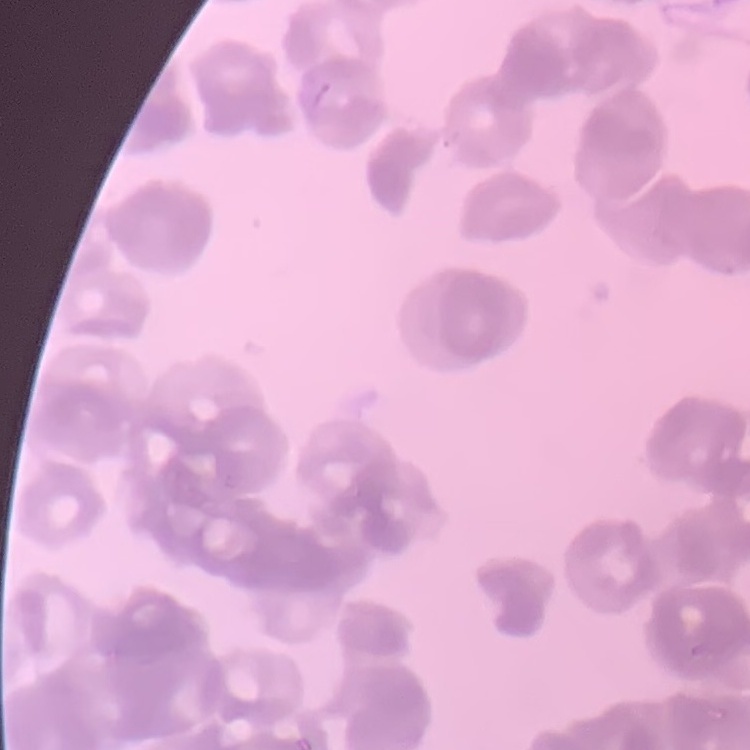
{
  "erythrocyte_morphology": "rouleaux formation",
  "preparation": "thin peripheral smear",
  "image_type": "square crop of a larger photomicrograph",
  "stain": "Field's or Giemsa"
}